Identify the parasite.
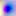

This is Toxoplasma gondii.

magnification = 400x
modality = micrograph